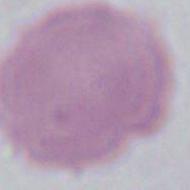
{
  "modality": "micrograph",
  "identification": "red blood cell",
  "magnification": "1000x"
}